Classify this cell by malaria status.
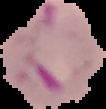
Parasitized.

From a thin blood film. Image is 106×109 pixels. The area outside the segmented cell region is set to black.